Describe the morphology of the erythrocytes.
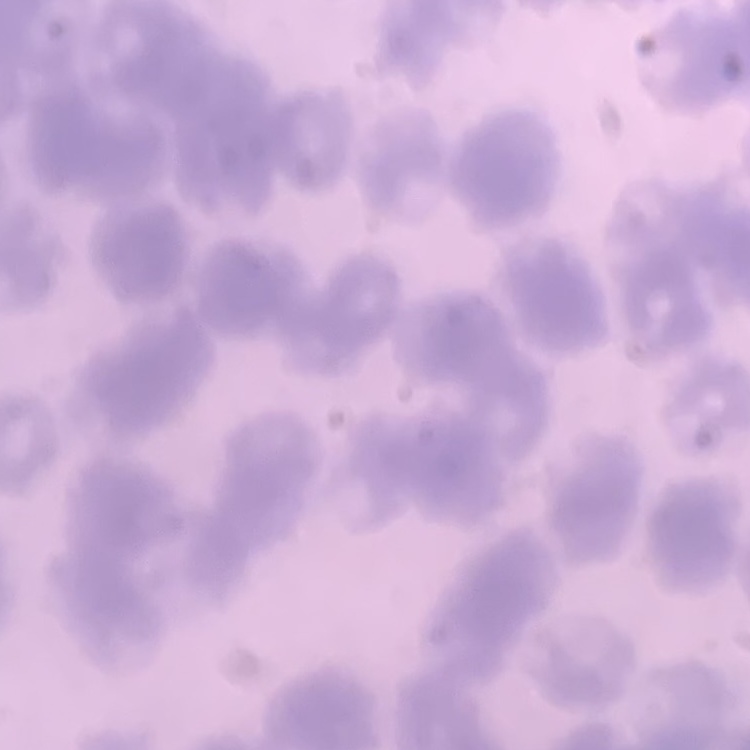
They show rouleaux formation.

Summary:
  - Image type: one tile cut from a larger photomicrograph
  - Preparation: thin blood film
  - Stain: Field's or Giemsa